Classify this cell by malaria status.
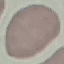
It is uninfected.

preparation: thin blood film
capture: smartphone through the microscope eyepiece
image_type: cell patch, automatically extracted from a larger field of view and resized to 64 × 64 pixels
stain: Giemsa